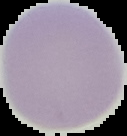
image_type: cell region segmented out of the field of view; surrounding area masked to black
preparation: thin blood smear
result: no Plasmodium parasites detected
image_size: 127×136 pixels